Give the extent of all Babesia divergens-infected red blood cells.
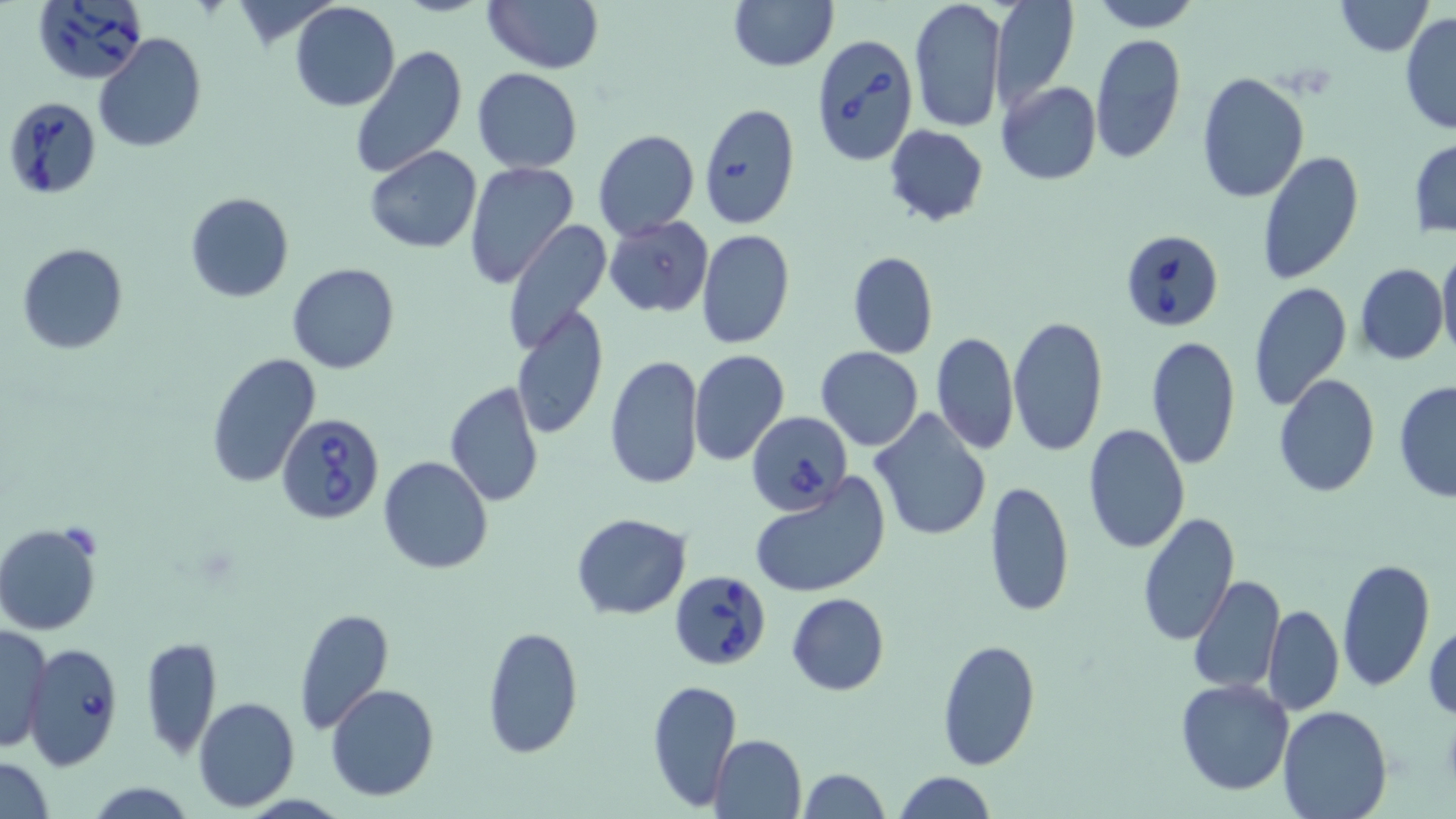
Approximate bounding boxes as named x1/y1/x2/y2 corners in pixels.
Babesia divergens-infected red blood cells: (x1=31, y1=0, x2=149, y2=86), (x1=811, y1=33, x2=918, y2=168), (x1=5, y1=94, x2=103, y2=198), (x1=1118, y1=229, x2=1224, y2=334), (x1=747, y1=410, x2=851, y2=516), (x1=277, y1=414, x2=388, y2=523), (x1=668, y1=569, x2=774, y2=671), (x1=21, y1=643, x2=125, y2=771).

slide_level_diagnosis: Babesia divergens
field_of_view: single
modality: light microscopy
preparation: thin blood smear
magnification: 1000x
image_size: 1456×819 pixels
uninfected_red_blood_cell_locations: 'approximate bounding boxes as named x1/y1/x2/y2 corners in pixels: (x1=229, y1=0, x2=333, y2=45), (x1=481, y1=0, x2=602, y2=73), (x1=727, y1=0, x2=837, y2=71), (x1=1089, y1=0, x2=1201, y2=31), (x1=1334, y1=0, x2=1432, y2=57), (x1=908, y1=1, x2=1007, y2=136), (x1=990, y1=1, x2=1077, y2=108), (x1=289, y1=3, x2=400, y2=112), (x1=1398, y1=12, x2=1456, y2=136), (x1=93, y1=32, x2=207, y2=153), (x1=1088, y1=34, x2=1185, y2=165), (x1=348, y1=44, x2=468, y2=179), (x1=472, y1=67, x2=583, y2=172), (x1=1194, y1=71, x2=1310, y2=204), (x1=996, y1=81, x2=1103, y2=185), (x1=699, y1=104, x2=801, y2=228), (x1=884, y1=124, x2=988, y2=226), (x1=593, y1=128, x2=699, y2=240), (x1=1409, y1=139, x2=1456, y2=237), (x1=363, y1=146, x2=484, y2=254), (x1=1258, y1=148, x2=1362, y2=286), (x1=464, y1=161, x2=579, y2=288), (x1=184, y1=190, x2=294, y2=304), (x1=604, y1=215, x2=713, y2=317), (x1=502, y1=221, x2=615, y2=356), (x1=696, y1=229, x2=795, y2=349), (x1=17, y1=243, x2=128, y2=354), (x1=1437, y1=244, x2=1456, y2=359), (x1=848, y1=251, x2=939, y2=359), (x1=287, y1=262, x2=401, y2=375), (x1=1355, y1=262, x2=1448, y2=366), (x1=1248, y1=281, x2=1352, y2=410), (x1=512, y1=306, x2=608, y2=440), (x1=1007, y1=314, x2=1109, y2=457), (x1=931, y1=331, x2=1018, y2=456), (x1=1143, y1=336, x2=1241, y2=470), (x1=816, y1=346, x2=923, y2=451), (x1=688, y1=349, x2=788, y2=466), (x1=206, y1=352, x2=321, y2=487), (x1=604, y1=354, x2=705, y2=490), (x1=1272, y1=373, x2=1380, y2=497), (x1=1393, y1=381, x2=1456, y2=503), (x1=444, y1=382, x2=545, y2=507), (x1=869, y1=408, x2=994, y2=541), (x1=1083, y1=424, x2=1189, y2=554), (x1=377, y1=454, x2=493, y2=576), (x1=749, y1=474, x2=891, y2=599), (x1=984, y1=479, x2=1075, y2=619), (x1=570, y1=511, x2=693, y2=619), (x1=1135, y1=511, x2=1241, y2=647), (x1=1, y1=522, x2=105, y2=636), (x1=1336, y1=557, x2=1436, y2=693), (x1=1187, y1=574, x2=1285, y2=693), (x1=786, y1=592, x2=890, y2=695), (x1=1262, y1=603, x2=1343, y2=716), (x1=294, y1=608, x2=394, y2=733), (x1=1425, y1=619, x2=1456, y2=723), (x1=1, y1=624, x2=51, y2=756), (x1=481, y1=624, x2=585, y2=759), (x1=140, y1=634, x2=222, y2=760), (x1=938, y1=638, x2=1040, y2=770), (x1=1175, y1=677, x2=1295, y2=796), (x1=647, y1=678, x2=742, y2=812), (x1=325, y1=683, x2=442, y2=801), (x1=193, y1=696, x2=300, y2=810), (x1=1276, y1=706, x2=1394, y2=819), (x1=708, y1=734, x2=806, y2=819), (x1=0, y1=756, x2=55, y2=818), (x1=797, y1=767, x2=891, y2=819), (x1=892, y1=772, x2=998, y2=817), (x1=84, y1=780, x2=198, y2=818)'
stain: May-Grünwald-Giemsa